Comment on the morphology of the red blood cells.
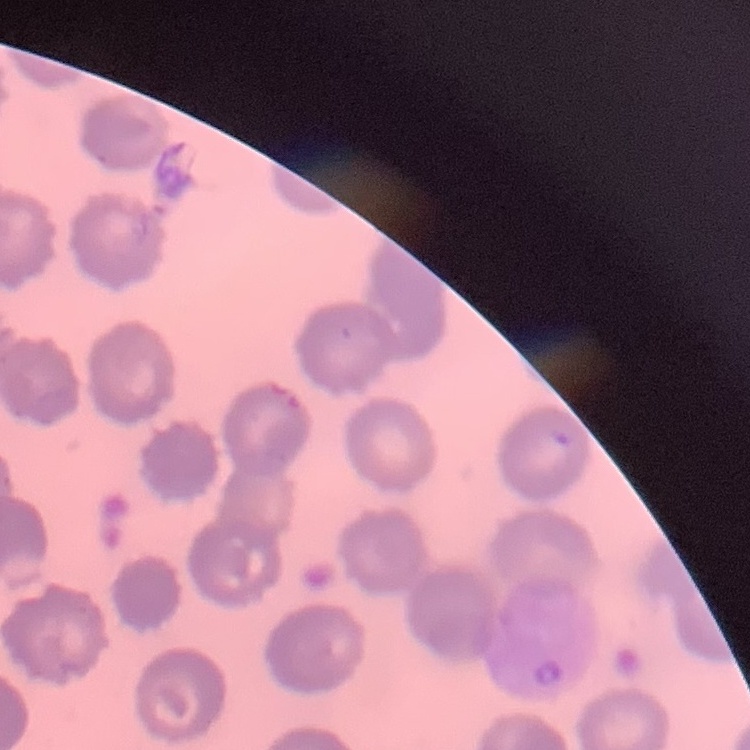
No rouleaux formation.

Summary:
  - Stain: Field's or Giemsa
  - Image type: square crop of a larger photomicrograph
  - Preparation: thin blood smear